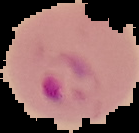
Result: malaria parasites detected. Image is 139×133 pixels. From a thin blood smear. Segmented cell region on a black background.